Classify this cell by malaria status.
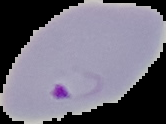
Parasitized.

preparation: thin blood smear
image_size: 166×124 pixels
image_type: cell region segmented out of the field of view; surrounding area masked to black